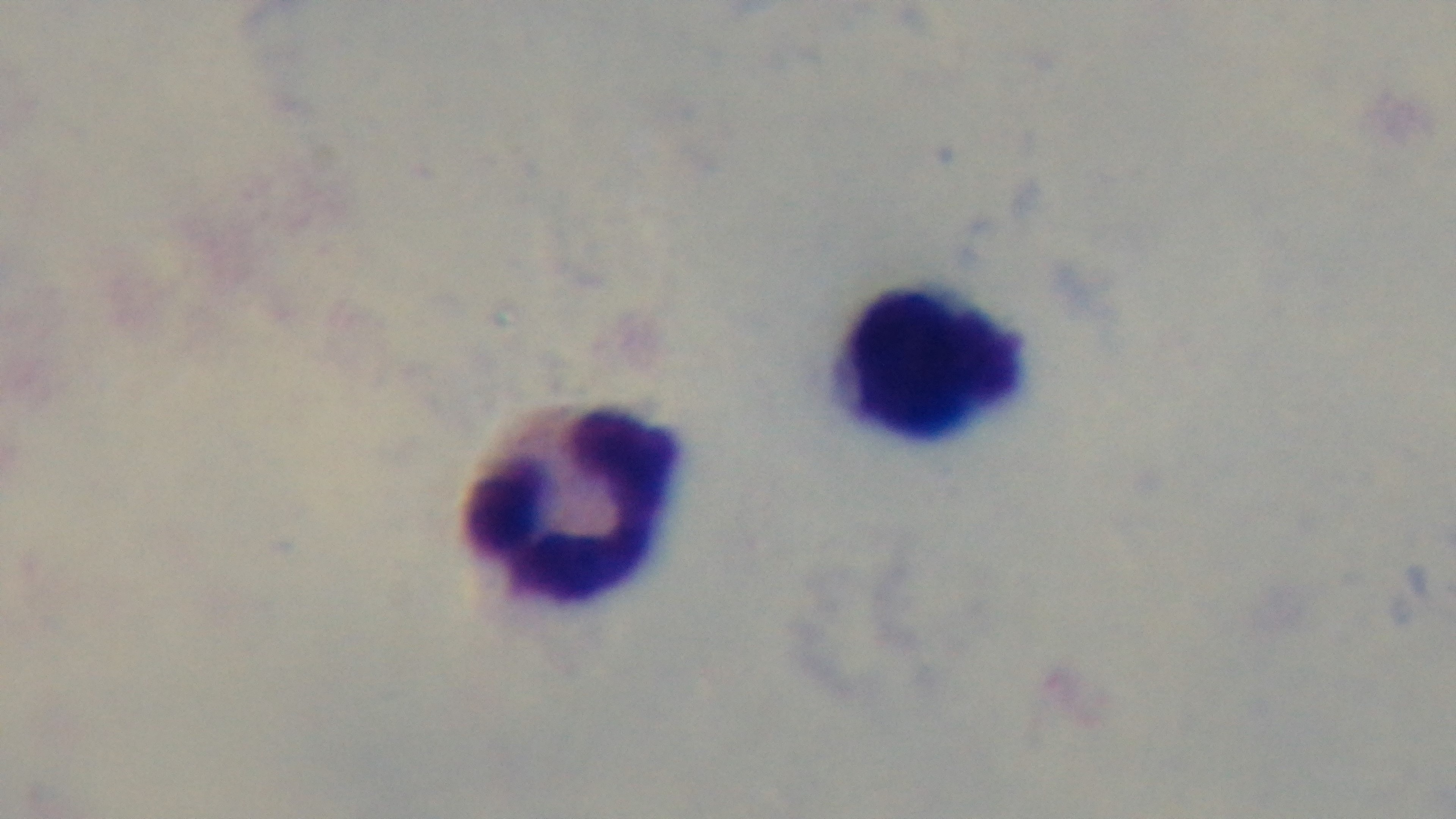

stain: Giemsa
field_of_view: one from the slide
preparation: thick smear
malaria_status: uninfected
objective: 100x oil immersion
capture: mounted 4K digital camera
modality: light microscopy